Locate every Plasmodium parasite.
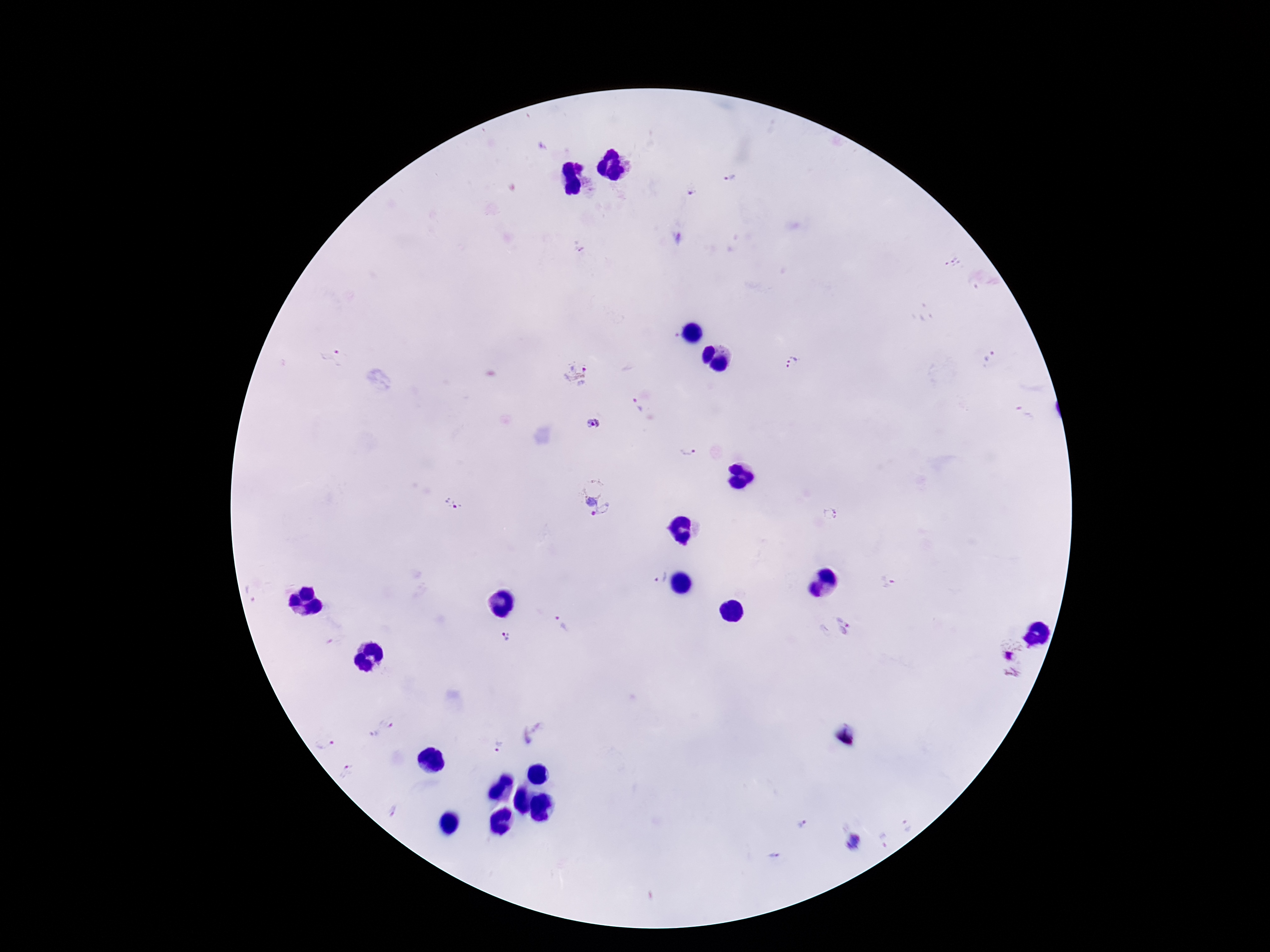
Approximate object centers, in pixels from the top-left corner.
Plasmodium parasites: (x=729, y=178), (x=692, y=191), (x=952, y=261), (x=991, y=355), (x=331, y=357), (x=792, y=362), (x=577, y=377), (x=636, y=404), (x=1024, y=413), (x=592, y=425), (x=689, y=449), (x=592, y=497), (x=453, y=504), (x=830, y=514), (x=661, y=577), (x=887, y=581), (x=255, y=592), (x=559, y=624), (x=833, y=627), (x=507, y=636), (x=1010, y=652), (x=1012, y=673), (x=382, y=729), (x=535, y=733), (x=325, y=745), (x=499, y=745), (x=346, y=771), (x=395, y=810), (x=804, y=823), (x=907, y=825), (x=885, y=841), (x=854, y=842), (x=774, y=855).

Summary:
  - Capture: smartphone camera through the microscope eyepiece
  - Stain: Giemsa
  - Image size: 1270×952 pixels
  - Field of view: single
  - Magnification: 100x
  - Preparation: thick blood film
  - Patient malaria status: positive